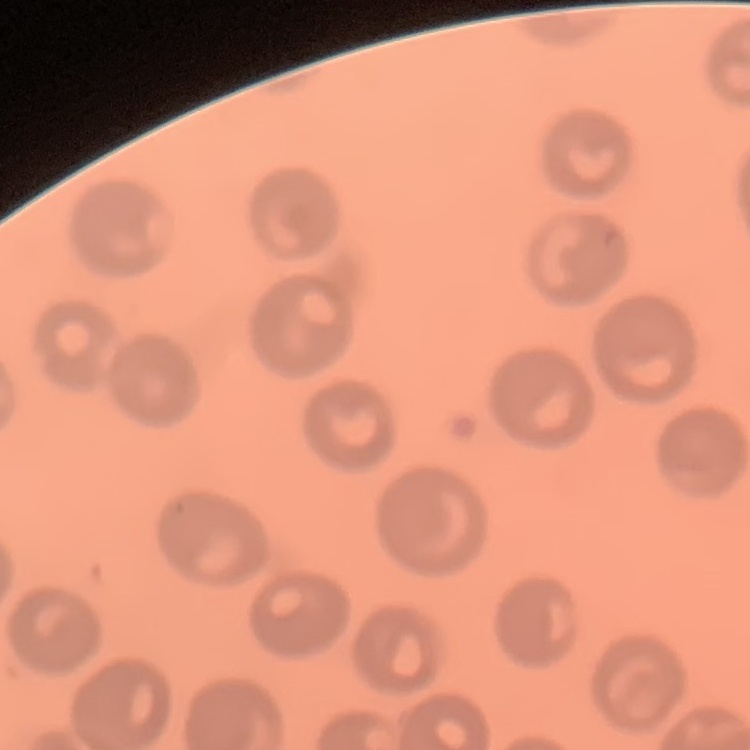

erythrocyte morphology = no rouleaux formation
image type = square crop of a larger photomicrograph
stain = Field's or Giemsa
preparation = thin blood smear